Identify the parasite.
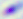
Toxoplasma gondii.

Summary:
  - Magnification: 400x
  - Modality: photomicrograph